Outline each blood parasite and name the species.
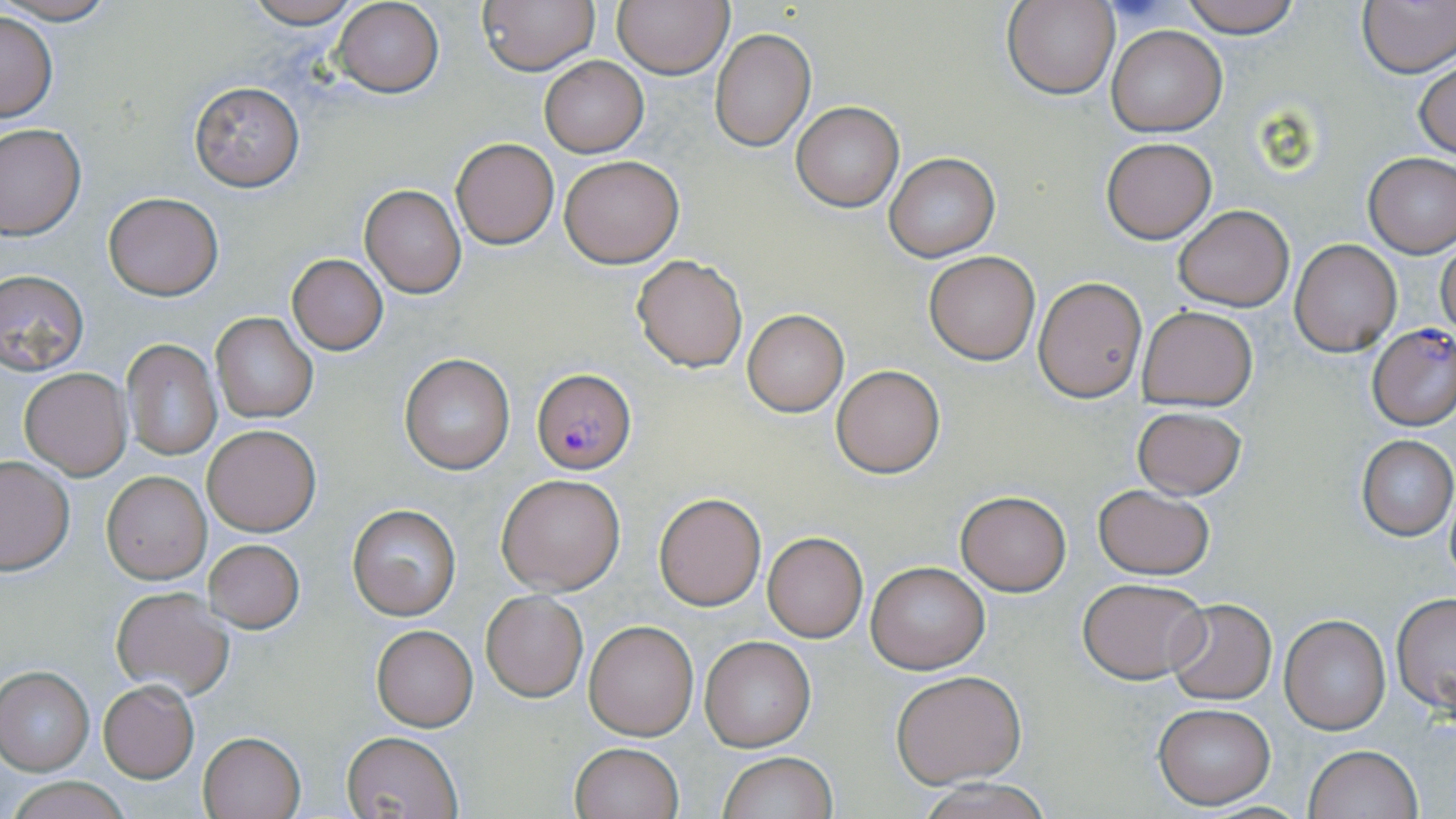

Approximate bounding boxes as named x1/y1/x2/y2 corners in pixels.
Plasmodium falciparum-infected red blood cells: (x1=1368, y1=325, x2=1456, y2=431), (x1=529, y1=367, x2=635, y2=473).
No Plasmodium ovale, Plasmodium malariae, Plasmodium vivax, Babesia divergens, or Trypanosoma brucei observed.

slide-level diagnosis = Plasmodium falciparum
image size = 1456×819 pixels
modality = light microscopy
uninfected red blood cell locations = approximate bounding boxes as named x1/y1/x2/y2 corners in pixels: (x1=1, y1=0, x2=118, y2=24), (x1=240, y1=0, x2=364, y2=28), (x1=477, y1=0, x2=598, y2=75), (x1=613, y1=0, x2=733, y2=77), (x1=1177, y1=0, x2=1303, y2=39), (x1=1356, y1=0, x2=1456, y2=78), (x1=332, y1=1, x2=443, y2=97), (x1=1005, y1=1, x2=1118, y2=99), (x1=631, y1=4, x2=779, y2=108), (x1=1, y1=12, x2=57, y2=123), (x1=1107, y1=25, x2=1227, y2=137), (x1=710, y1=27, x2=816, y2=151), (x1=540, y1=57, x2=647, y2=156), (x1=1414, y1=59, x2=1456, y2=159), (x1=189, y1=81, x2=305, y2=193), (x1=791, y1=102, x2=904, y2=212), (x1=0, y1=124, x2=86, y2=240), (x1=1101, y1=137, x2=1217, y2=244), (x1=450, y1=138, x2=560, y2=249), (x1=1363, y1=152, x2=1456, y2=259), (x1=884, y1=153, x2=1000, y2=261), (x1=560, y1=156, x2=683, y2=267), (x1=359, y1=183, x2=466, y2=298), (x1=104, y1=192, x2=223, y2=300), (x1=1173, y1=205, x2=1292, y2=312), (x1=1290, y1=239, x2=1400, y2=356), (x1=1437, y1=240, x2=1456, y2=339), (x1=924, y1=250, x2=1040, y2=364), (x1=287, y1=254, x2=388, y2=355), (x1=631, y1=254, x2=748, y2=372), (x1=0, y1=268, x2=89, y2=374), (x1=1032, y1=275, x2=1147, y2=402), (x1=1137, y1=305, x2=1259, y2=411), (x1=742, y1=310, x2=848, y2=416), (x1=212, y1=314, x2=317, y2=423), (x1=121, y1=338, x2=223, y2=462), (x1=400, y1=354, x2=515, y2=474), (x1=832, y1=364, x2=945, y2=478), (x1=20, y1=368, x2=131, y2=479), (x1=1132, y1=405, x2=1247, y2=500), (x1=202, y1=425, x2=322, y2=536), (x1=1356, y1=435, x2=1455, y2=540), (x1=0, y1=456, x2=74, y2=575), (x1=100, y1=469, x2=211, y2=584), (x1=497, y1=473, x2=624, y2=594), (x1=1092, y1=484, x2=1213, y2=580), (x1=955, y1=490, x2=1071, y2=595), (x1=1443, y1=490, x2=1456, y2=587), (x1=654, y1=493, x2=766, y2=611), (x1=347, y1=503, x2=462, y2=620), (x1=762, y1=532, x2=867, y2=642), (x1=202, y1=540, x2=305, y2=634), (x1=866, y1=562, x2=990, y2=674), (x1=1076, y1=577, x2=1210, y2=683), (x1=109, y1=587, x2=234, y2=699), (x1=481, y1=591, x2=587, y2=702), (x1=1391, y1=594, x2=1456, y2=711), (x1=1166, y1=599, x2=1276, y2=704), (x1=1279, y1=613, x2=1391, y2=736), (x1=584, y1=620, x2=698, y2=740), (x1=371, y1=624, x2=478, y2=731), (x1=699, y1=636, x2=817, y2=752), (x1=0, y1=666, x2=93, y2=774), (x1=892, y1=672, x2=1025, y2=787), (x1=98, y1=681, x2=199, y2=782), (x1=1153, y1=703, x2=1275, y2=808), (x1=342, y1=731, x2=463, y2=818), (x1=197, y1=732, x2=305, y2=818), (x1=569, y1=741, x2=685, y2=819), (x1=1304, y1=745, x2=1421, y2=819), (x1=717, y1=751, x2=836, y2=819), (x1=10, y1=776, x2=131, y2=819), (x1=918, y1=779, x2=1059, y2=819)
stain = May-Grünwald-Giemsa
field of view = single
preparation = thin blood smear
magnification = 1000x